Evaluate for Plasmodium parasites.
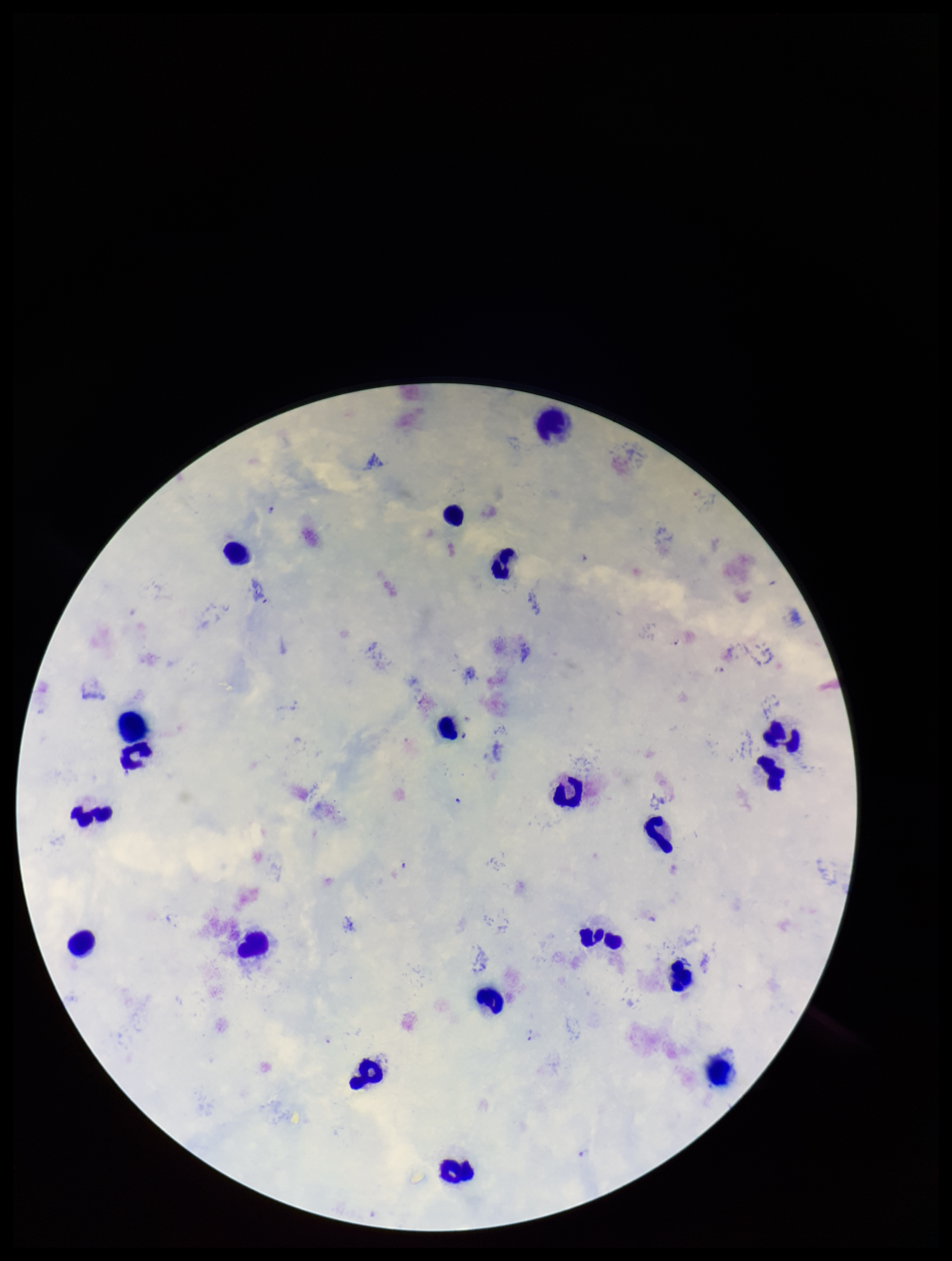

Seen.

{
  "stain": "Giemsa",
  "image_size": "952×1261 pixels",
  "field_of_view": "one from this slide",
  "patient_malaria_status": "positive",
  "capture": "smartphone photograph through the microscope eyepiece",
  "preparation": "thick blood smear",
  "leukocyte_count": 20,
  "species_reported_for_this_patient": "Plasmodium falciparum",
  "parasite_count": 4
}